Classify this cell by malaria status.
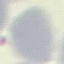

Uninfected.

Summary:
  - Capture: smartphone camera at the microscope eyepiece
  - Stain: Giemsa
  - Image type: automatically extracted cell patch, resized to 64 × 64 pixels
  - Preparation: thin smear